Report the malaria status of this cell.
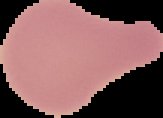

It is uninfected.

Summary:
  - Image type: cell region segmented out of the field of view; surrounding area masked to black
  - Image size: 163×118 pixels
  - Preparation: thin blood smear